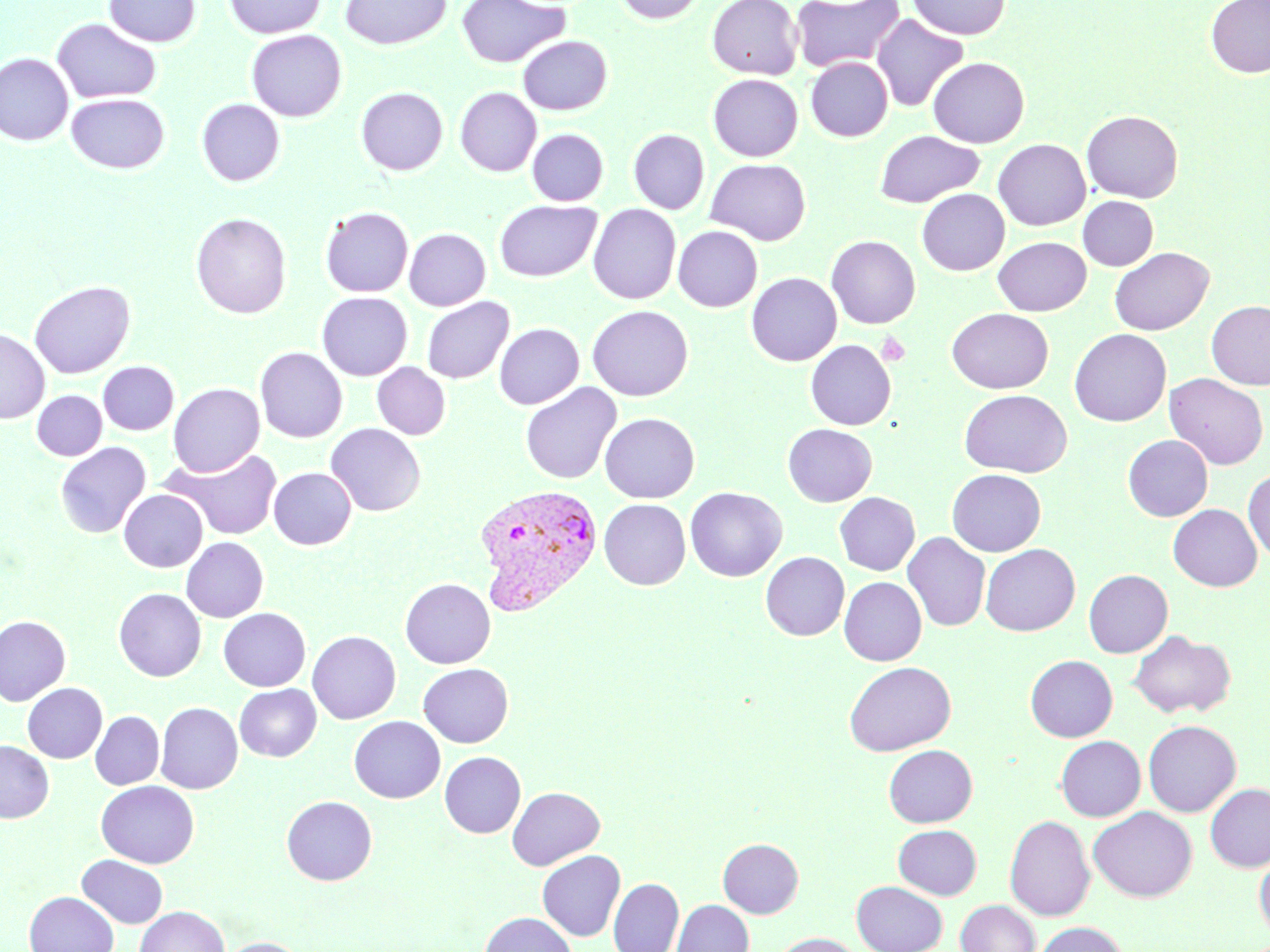
slide_level_diagnosis: Plasmodium vivax
stain: May-Grünwald-Giemsa
field_of_view: single
platelet_locations: 'approximate bounding boxes as (x1, y1, x2, y2) in pixels: (876, 332, 911, 366)'
modality: light microscopy
magnification: 1000x
image_size: 1270×952 pixels
plasmodium_vivax_infected_red_blood_cell_locations: 'approximate bounding boxes as (x1, y1, x2, y2) in pixels: (472, 483, 604, 616)'
preparation: thin blood smear
uninfected_red_blood_cell_locations: 'approximate bounding boxes as (x1, y1, x2, y2) in pixels: (104, 0, 201, 47), (224, 0, 324, 38), (340, 0, 452, 50), (456, 0, 570, 68), (614, 0, 706, 24), (707, 0, 802, 79), (790, 0, 904, 72), (909, 0, 1010, 39), (1206, 0, 1270, 78), (871, 13, 969, 113), (52, 18, 161, 103), (246, 29, 347, 121), (518, 36, 613, 115), (0, 52, 73, 146), (806, 57, 893, 141), (928, 57, 1029, 148), (708, 74, 802, 161), (355, 86, 448, 175), (455, 87, 541, 176), (66, 93, 170, 174), (196, 98, 285, 186), (1081, 109, 1183, 202), (527, 128, 608, 205), (628, 129, 709, 214), (875, 130, 984, 208), (993, 139, 1090, 231), (705, 158, 811, 245), (917, 188, 1009, 276), (1078, 196, 1158, 271), (494, 199, 601, 282), (588, 203, 681, 304), (320, 206, 413, 297), (191, 212, 292, 319), (673, 225, 763, 312), (404, 228, 490, 310), (826, 235, 920, 328), (993, 237, 1091, 316), (1109, 246, 1214, 335), (746, 272, 842, 366), (28, 280, 135, 378), (316, 292, 412, 381), (421, 296, 514, 384), (1206, 301, 1270, 390), (587, 305, 693, 401), (947, 307, 1053, 394), (494, 323, 584, 409), (0, 328, 50, 423), (1069, 328, 1171, 427), (805, 339, 896, 430), (255, 347, 347, 442), (98, 361, 179, 435), (372, 362, 451, 440), (1164, 373, 1269, 470), (520, 382, 621, 484), (168, 383, 265, 477), (959, 389, 1072, 477), (32, 390, 107, 461), (599, 412, 699, 502), (325, 423, 425, 516), (782, 423, 876, 506), (1123, 434, 1213, 521), (55, 442, 152, 538), (163, 447, 283, 540), (269, 467, 356, 549), (947, 469, 1045, 556), (1243, 469, 1270, 561), (684, 487, 787, 582), (119, 489, 208, 572), (835, 492, 919, 575), (599, 498, 690, 589), (1168, 504, 1263, 591), (902, 532, 990, 632), (181, 537, 269, 622), (980, 544, 1080, 636), (760, 552, 849, 640), (1084, 569, 1173, 657), (839, 576, 926, 666), (400, 577, 496, 669), (114, 588, 206, 682), (218, 607, 311, 691), (0, 615, 71, 707), (307, 630, 401, 724), (1128, 630, 1235, 718), (1025, 655, 1117, 742), (843, 661, 956, 755), (417, 663, 514, 747), (23, 682, 107, 763), (234, 684, 321, 762), (156, 702, 243, 794), (90, 711, 164, 789), (349, 716, 445, 804), (1143, 720, 1241, 816), (1055, 736, 1145, 821), (0, 740, 54, 823), (883, 744, 977, 827), (440, 751, 525, 838), (96, 780, 199, 868), (1205, 784, 1270, 871), (506, 786, 605, 870), (281, 796, 377, 885), (1089, 806, 1197, 902), (1005, 814, 1095, 921), (893, 824, 982, 899), (718, 838, 804, 918), (537, 850, 625, 941), (1255, 851, 1270, 940), (77, 855, 168, 929), (608, 878, 684, 952), (852, 881, 947, 952), (24, 891, 119, 952), (672, 900, 753, 952), (956, 900, 1040, 952), (134, 906, 230, 952), (479, 911, 577, 952), (1034, 922, 1128, 952), (772, 933, 863, 952), (217, 937, 308, 952)'